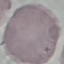
result = no malaria parasites seen
capture = smartphone camera at the microscope eyepiece
stain = Giemsa
preparation = thin blood smear
image type = automatically extracted cell patch, resized to 64 × 64 pixels